Identify the parasite.
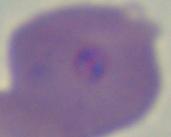

This is Babesia.

{
  "magnification": "1000x",
  "modality": "photomicrograph"
}